Outline each blood parasite and name the species.
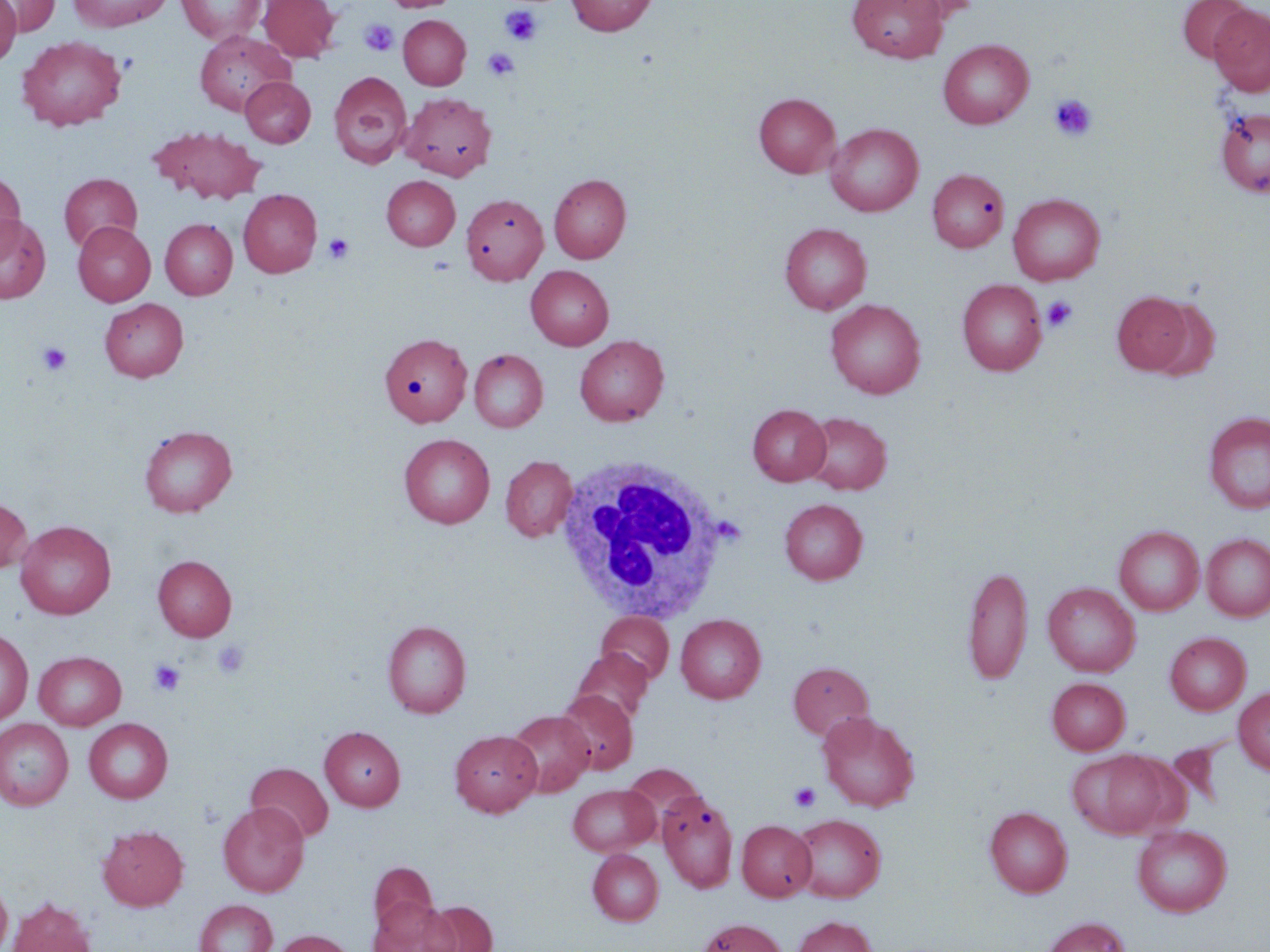

No blood parasites seen.

Summary:
  - Coordinate format: approximate bounding boxes as [x1, y1, x2, y2] in pixels
  - Uninfected red blood cell locations: [0, 0, 21, 67], [1, 0, 59, 36], [69, 0, 172, 32], [176, 0, 265, 44], [259, 0, 340, 62], [386, 0, 458, 12], [566, 0, 658, 36], [848, 0, 947, 63], [888, 0, 982, 23], [1177, 0, 1253, 63], [1209, 4, 1270, 96], [398, 15, 470, 90], [195, 30, 295, 115], [16, 35, 127, 131], [938, 39, 1033, 129], [328, 71, 412, 169], [240, 77, 315, 147], [400, 92, 496, 180], [754, 93, 840, 177], [1217, 107, 1270, 197], [826, 124, 923, 216], [149, 126, 266, 205], [927, 168, 1009, 252], [0, 172, 26, 258], [59, 173, 142, 252], [549, 174, 631, 263], [382, 176, 460, 250], [239, 189, 322, 277], [460, 193, 548, 285], [1008, 193, 1105, 285], [0, 214, 51, 303], [160, 219, 237, 300], [73, 221, 155, 306], [780, 223, 872, 314], [526, 265, 613, 350], [957, 278, 1048, 375], [1112, 291, 1195, 376], [1145, 297, 1221, 380], [100, 298, 188, 381], [826, 299, 925, 398], [380, 334, 472, 425], [575, 335, 669, 425], [469, 349, 547, 432], [748, 404, 830, 485], [801, 412, 892, 495], [1204, 412, 1270, 514], [138, 425, 237, 517], [399, 433, 495, 528], [500, 455, 577, 542], [0, 498, 32, 574], [780, 499, 867, 584], [16, 520, 116, 619], [1114, 526, 1204, 615], [1201, 533, 1270, 622], [153, 555, 236, 641], [962, 563, 1032, 685], [1043, 582, 1140, 677], [597, 612, 674, 685], [676, 614, 765, 703], [383, 620, 471, 718], [0, 628, 33, 725], [1165, 632, 1251, 715], [572, 648, 652, 725], [34, 651, 126, 730], [788, 661, 874, 740], [1047, 678, 1130, 754], [1233, 687, 1270, 775], [555, 690, 638, 774], [507, 710, 594, 797], [817, 712, 919, 812], [84, 718, 173, 803], [0, 719, 73, 810], [319, 726, 405, 811], [450, 729, 541, 816], [1067, 749, 1177, 839], [247, 763, 333, 842], [622, 763, 706, 839], [568, 784, 659, 856], [657, 791, 739, 893], [218, 802, 309, 897], [984, 806, 1072, 897], [790, 813, 886, 902], [737, 820, 816, 901], [97, 824, 188, 911], [1132, 824, 1232, 917], [587, 849, 663, 925], [368, 862, 438, 938], [0, 878, 12, 950], [7, 897, 97, 952], [370, 898, 458, 952], [194, 900, 277, 952], [423, 901, 496, 952], [793, 916, 877, 952], [1042, 917, 1130, 952], [696, 918, 788, 952], [271, 930, 356, 952]
  - Platelet locations: [501, 6, 542, 46], [359, 19, 398, 57], [482, 47, 519, 80], [1049, 94, 1096, 142], [323, 233, 354, 264], [1042, 296, 1078, 332], [37, 342, 72, 376], [212, 640, 250, 679], [149, 660, 185, 696], [789, 782, 821, 812]
  - White blood cell locations: [555, 457, 736, 624]
  - Slide-level diagnosis: negative for blood parasites
  - Preparation: thin blood film
  - Field of view: one of a larger specimen
  - Image size: 1270×952 pixels
  - Magnification: 1000x
  - Modality: optical microscopy
  - Stain: May-Grünwald-Giemsa